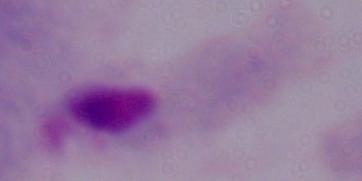
A trichomonad is seen. 1000x magnification. Micrograph.